Evaluate for malaria.
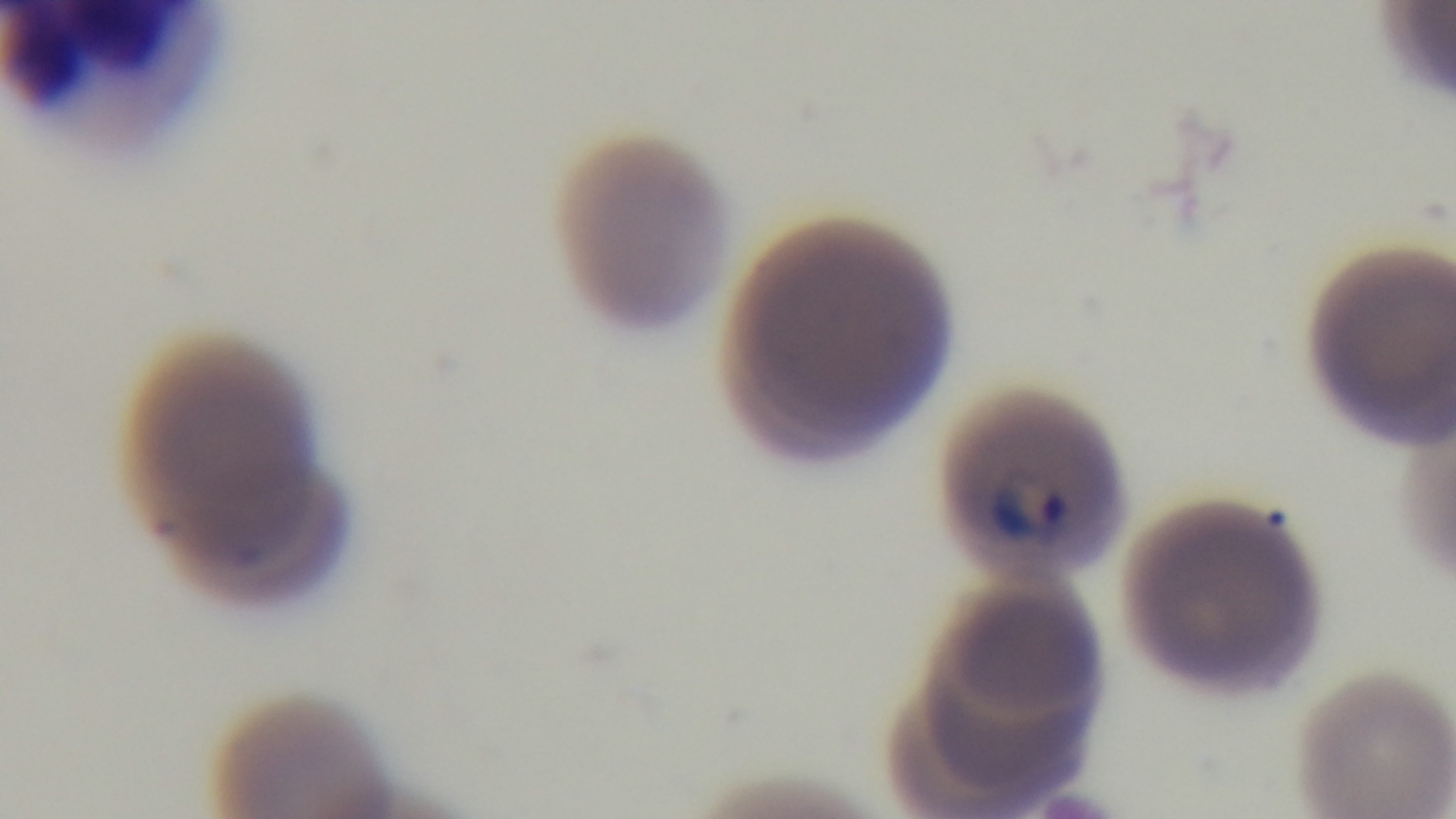

It is infected.

Summary:
  - Modality: light microscopy
  - Field of view: single
  - Capture: mounted 4K digital camera
  - Stain: Giemsa
  - Objective: 100x oil immersion
  - Preparation: thin smear